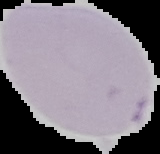

result = no malaria parasites detected
image type = cell region segmented out of the field of view; surrounding area masked to black
preparation = thin blood smear
image size = 160×154 pixels